Assess this cell for malaria.
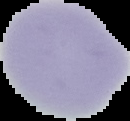
Uninfected.

image_size: 130×121 pixels
image_type: segmented cell region on a black background
preparation: thin blood smear